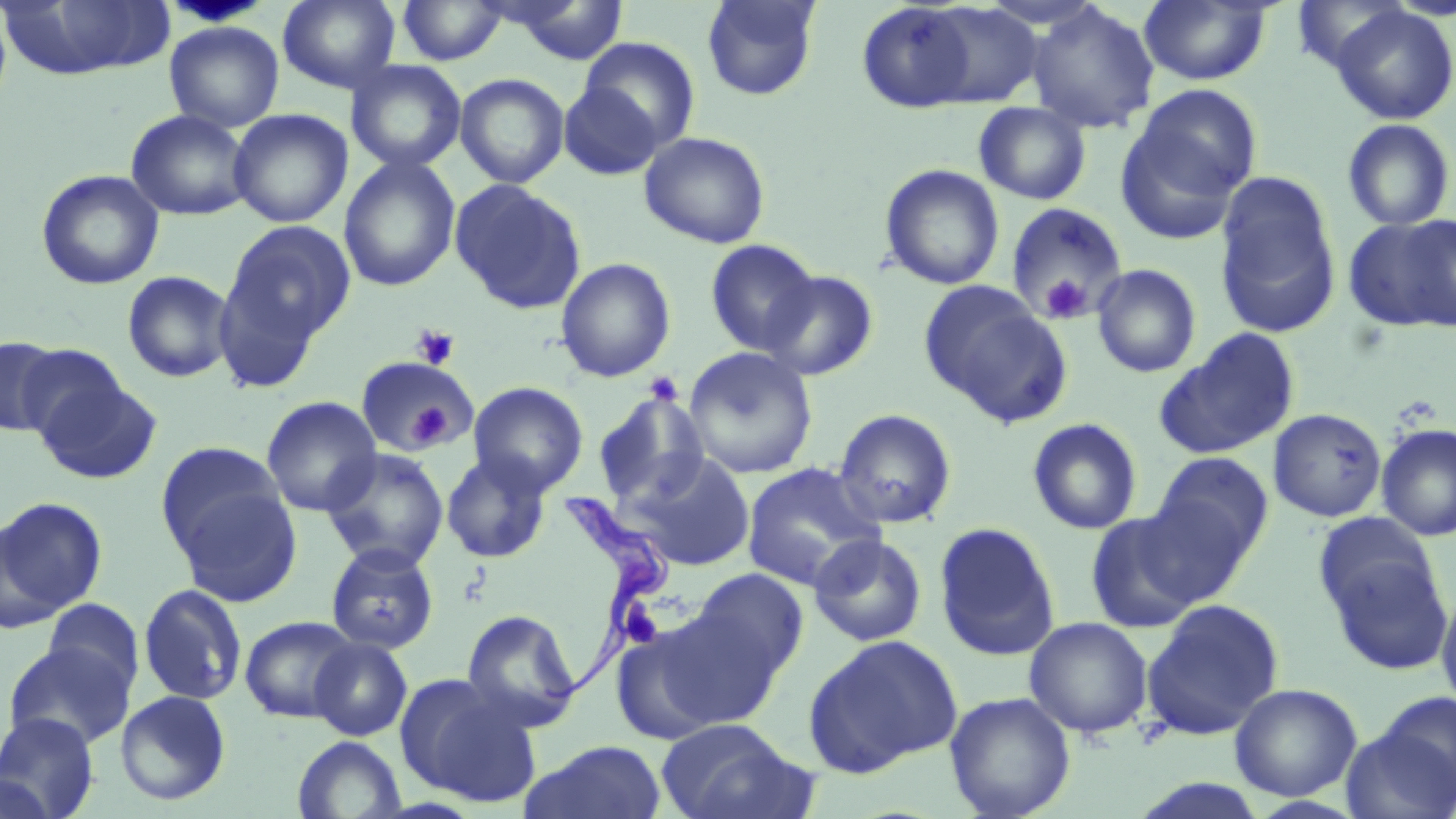 Approximate bounding boxes as named x1/y1/x2/y2 corners in pixels. Trypanosoma brucei locations: (x1=537, y1=489, x2=677, y2=719). Uninfected red blood cell locations (subset): (x1=277, y1=0, x2=401, y2=93), (x1=501, y1=0, x2=630, y2=65), (x1=701, y1=0, x2=820, y2=101), (x1=1139, y1=0, x2=1272, y2=86), (x1=1, y1=1, x2=177, y2=80), (x1=396, y1=1, x2=508, y2=66), (x1=1293, y1=1, x2=1408, y2=72), (x1=856, y1=2, x2=981, y2=113), (x1=921, y1=3, x2=1045, y2=108), (x1=1025, y1=3, x2=1160, y2=134), (x1=1330, y1=5, x2=1456, y2=125), (x1=164, y1=20, x2=284, y2=132), (x1=579, y1=37, x2=699, y2=151), (x1=346, y1=60, x2=467, y2=172), (x1=455, y1=73, x2=570, y2=188), (x1=559, y1=82, x2=663, y2=180), (x1=1118, y1=85, x2=1261, y2=235), (x1=973, y1=102, x2=1092, y2=205), (x1=228, y1=108, x2=352, y2=228), (x1=125, y1=109, x2=253, y2=221), (x1=1341, y1=118, x2=1455, y2=231), (x1=639, y1=131, x2=771, y2=249), (x1=338, y1=155, x2=461, y2=292), (x1=880, y1=164, x2=1004, y2=291), (x1=36, y1=169, x2=165, y2=290), (x1=1215, y1=174, x2=1341, y2=339), (x1=449, y1=178, x2=587, y2=315), (x1=1003, y1=202, x2=1128, y2=324), (x1=1343, y1=214, x2=1456, y2=334), (x1=220, y1=220, x2=357, y2=351), (x1=705, y1=239, x2=821, y2=356), (x1=555, y1=257, x2=676, y2=383), (x1=1091, y1=264, x2=1202, y2=378), (x1=122, y1=270, x2=236, y2=382), (x1=761, y1=270, x2=879, y2=381), (x1=920, y1=283, x2=1069, y2=425), (x1=1155, y1=328, x2=1300, y2=459), (x1=1, y1=338, x2=64, y2=436), (x1=16, y1=344, x2=131, y2=445), (x1=682, y1=346, x2=818, y2=479), (x1=355, y1=356, x2=482, y2=460), (x1=33, y1=372, x2=161, y2=484), (x1=468, y1=381, x2=588, y2=496), (x1=593, y1=391, x2=710, y2=508), (x1=261, y1=396, x2=382, y2=517), (x1=833, y1=408, x2=957, y2=529), (x1=1268, y1=408, x2=1387, y2=522), (x1=1027, y1=417, x2=1143, y2=535), (x1=1376, y1=423, x2=1455, y2=542), (x1=155, y1=441, x2=289, y2=562), (x1=321, y1=447, x2=449, y2=572), (x1=440, y1=452, x2=552, y2=564), (x1=1152, y1=452, x2=1273, y2=565), (x1=625, y1=453, x2=757, y2=571), (x1=741, y1=461, x2=886, y2=591), (x1=172, y1=484, x2=302, y2=607), (x1=0, y1=496, x2=106, y2=624), (x1=1084, y1=511, x2=1205, y2=633), (x1=933, y1=522, x2=1060, y2=662), (x1=808, y1=533, x2=928, y2=648), (x1=1322, y1=541, x2=1453, y2=675), (x1=325, y1=543, x2=440, y2=655), (x1=688, y1=568, x2=809, y2=682), (x1=139, y1=583, x2=247, y2=706), (x1=1436, y1=589, x2=1456, y2=716), (x1=42, y1=598, x2=145, y2=698), (x1=1141, y1=598, x2=1284, y2=741), (x1=652, y1=605, x2=787, y2=727), (x1=461, y1=609, x2=583, y2=732), (x1=240, y1=615, x2=359, y2=723), (x1=1023, y1=617, x2=1153, y2=738), (x1=609, y1=619, x2=731, y2=742), (x1=803, y1=633, x2=962, y2=776), (x1=309, y1=637, x2=413, y2=741), (x1=3, y1=642, x2=133, y2=751), (x1=395, y1=672, x2=543, y2=807), (x1=1229, y1=683, x2=1362, y2=801), (x1=115, y1=690, x2=231, y2=806), (x1=944, y1=691, x2=1076, y2=819), (x1=1373, y1=693, x2=1456, y2=802), (x1=0, y1=712, x2=100, y2=818), (x1=655, y1=718, x2=811, y2=819), (x1=292, y1=735, x2=407, y2=819), (x1=521, y1=740, x2=667, y2=818), (x1=0, y1=773, x2=57, y2=819), (x1=1128, y1=778, x2=1272, y2=819). Platelet locations (subset): (x1=1039, y1=274, x2=1092, y2=324), (x1=412, y1=325, x2=459, y2=370), (x1=643, y1=371, x2=684, y2=406), (x1=407, y1=400, x2=454, y2=449). Slide-level diagnosis: Trypanosoma brucei. Captured at 1000x magnification. One field of a larger specimen. Image is 1456×819 pixels. Thin blood smear. Light microscopy. May-Grünwald-Giemsa-stained preparation.